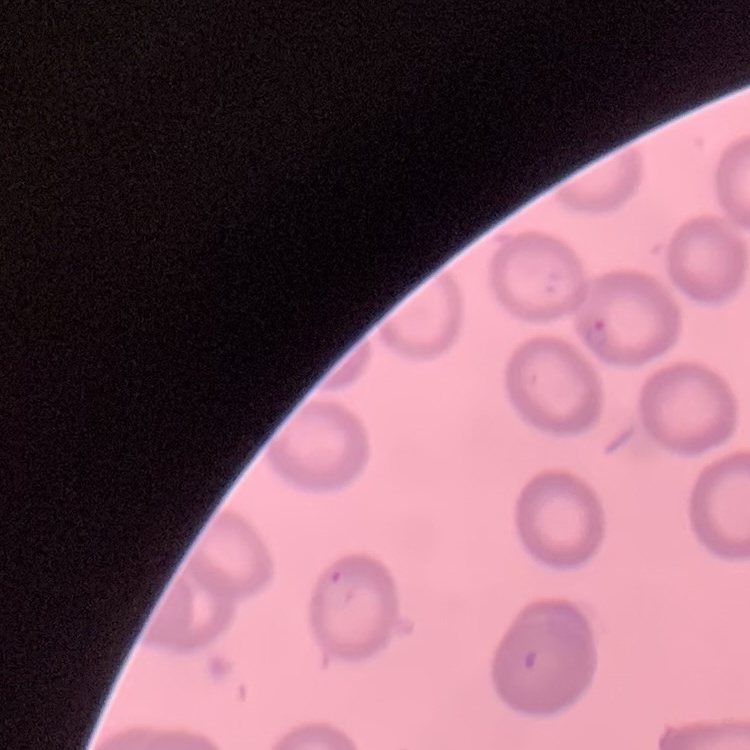

erythrocyte_morphology: no rouleaux formation
image_type: one tile cut from a larger photomicrograph
preparation: thin peripheral smear
stain: Field's or Giemsa